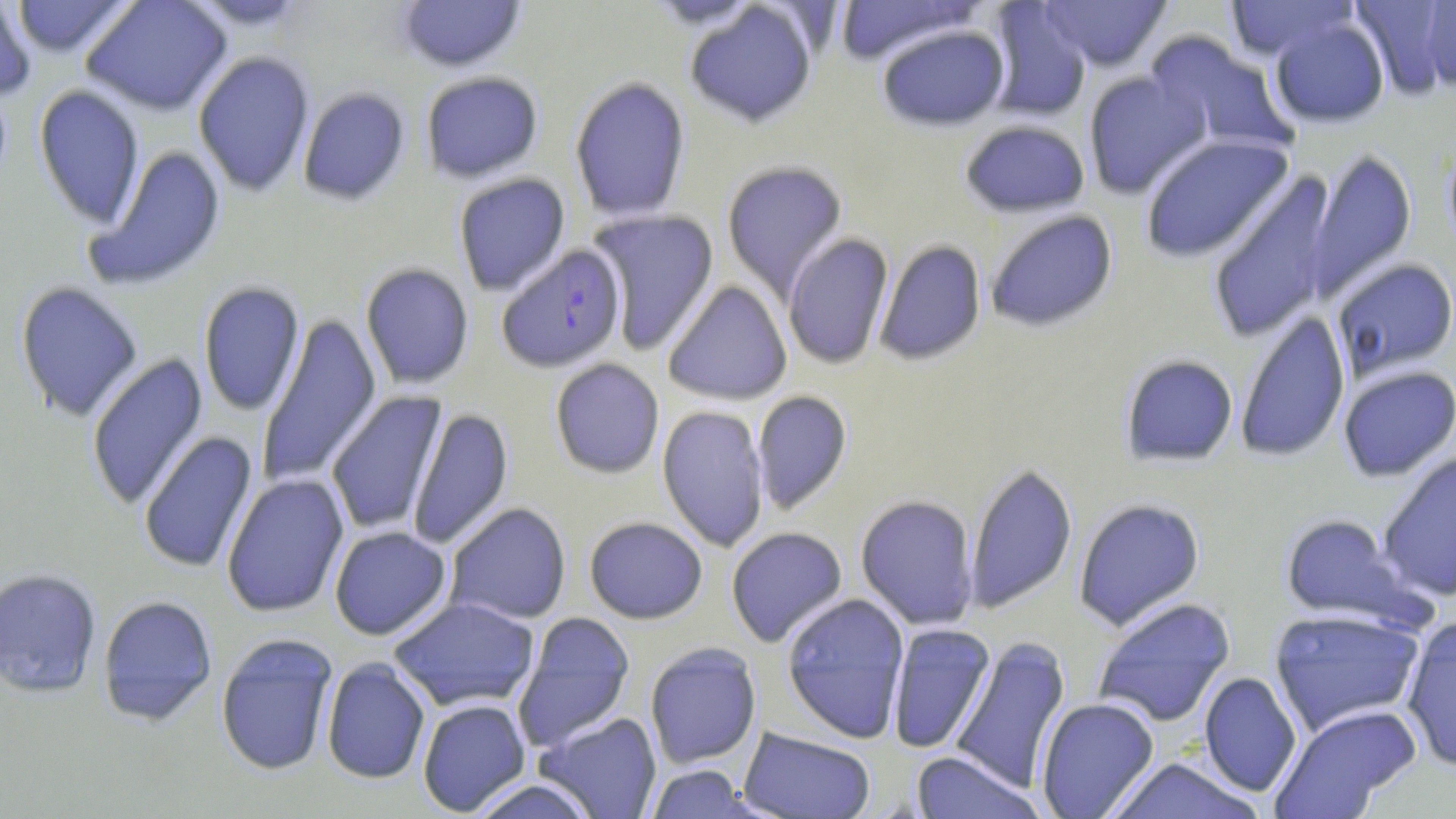
{
  "slide_level_diagnosis": "Plasmodium falciparum",
  "uninfected_red_blood_cell_locations": "approximate bounding boxes as [x1, y1, x2, y2] in pixels: [0, 0, 37, 103], [9, 0, 137, 58], [82, 0, 232, 116], [183, 0, 315, 30], [396, 0, 527, 72], [642, 0, 764, 29], [833, 0, 984, 66], [1038, 0, 1173, 72], [1225, 0, 1357, 62], [1349, 0, 1453, 99], [1419, 1, 1456, 92], [685, 2, 818, 127], [986, 2, 1092, 122], [1270, 18, 1390, 128], [876, 24, 1010, 131], [1144, 33, 1297, 157], [192, 51, 315, 196], [1082, 70, 1212, 199], [420, 71, 544, 183], [569, 75, 691, 224], [33, 85, 145, 228], [297, 87, 411, 205], [959, 119, 1090, 218], [1139, 134, 1295, 264], [1443, 140, 1456, 259], [84, 145, 227, 291], [1305, 149, 1417, 302], [721, 160, 848, 299], [1206, 171, 1338, 344], [453, 172, 571, 297], [587, 209, 720, 355], [985, 209, 1119, 332], [782, 232, 895, 371], [874, 239, 987, 366], [1331, 258, 1456, 380], [359, 263, 475, 389], [661, 280, 793, 405], [15, 281, 144, 422], [198, 281, 306, 416], [1235, 309, 1351, 463], [255, 314, 383, 489], [85, 353, 209, 512], [1120, 355, 1238, 467], [549, 358, 665, 479], [1338, 366, 1456, 481], [751, 390, 853, 515], [325, 391, 448, 536], [657, 404, 770, 552], [406, 407, 514, 551], [138, 431, 258, 574], [1377, 450, 1456, 602], [964, 462, 1077, 613], [221, 473, 350, 617], [855, 494, 979, 630], [1073, 497, 1205, 631], [444, 502, 572, 625], [1280, 512, 1419, 629], [584, 516, 708, 624], [329, 526, 452, 640], [725, 527, 848, 648], [0, 567, 102, 698], [782, 593, 910, 744], [97, 595, 218, 726], [1092, 596, 1236, 728], [387, 597, 541, 713], [1268, 607, 1427, 737], [512, 612, 635, 751], [1400, 614, 1456, 771], [885, 623, 996, 755], [215, 632, 339, 776], [949, 635, 1072, 795], [644, 642, 762, 768], [321, 658, 431, 784], [1198, 670, 1302, 797], [1035, 697, 1159, 818], [417, 699, 531, 816], [1269, 703, 1422, 818], [536, 710, 663, 818], [738, 727, 876, 818], [910, 751, 1045, 819], [1107, 757, 1265, 819], [645, 763, 757, 819], [465, 778, 599, 819]",
  "field_of_view": "single",
  "plasmodium_falciparum_infected_red_blood_cell_locations": "approximate bounding boxes as [x1, y1, x2, y2] in pixels: [496, 243, 628, 373]",
  "image_size": "1456×819 pixels",
  "modality": "light microscopy",
  "stain": "May-Grünwald-Giemsa",
  "preparation": "thin blood film",
  "magnification": "1000x"
}